Classify this cell by malaria status.
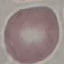
It is uninfected.

Summary:
  - Preparation: thin blood smear
  - Capture: smartphone through the microscope eyepiece
  - Stain: Giemsa
  - Image type: cell patch, automatically extracted from a larger field of view and resized to 64 × 64 pixels